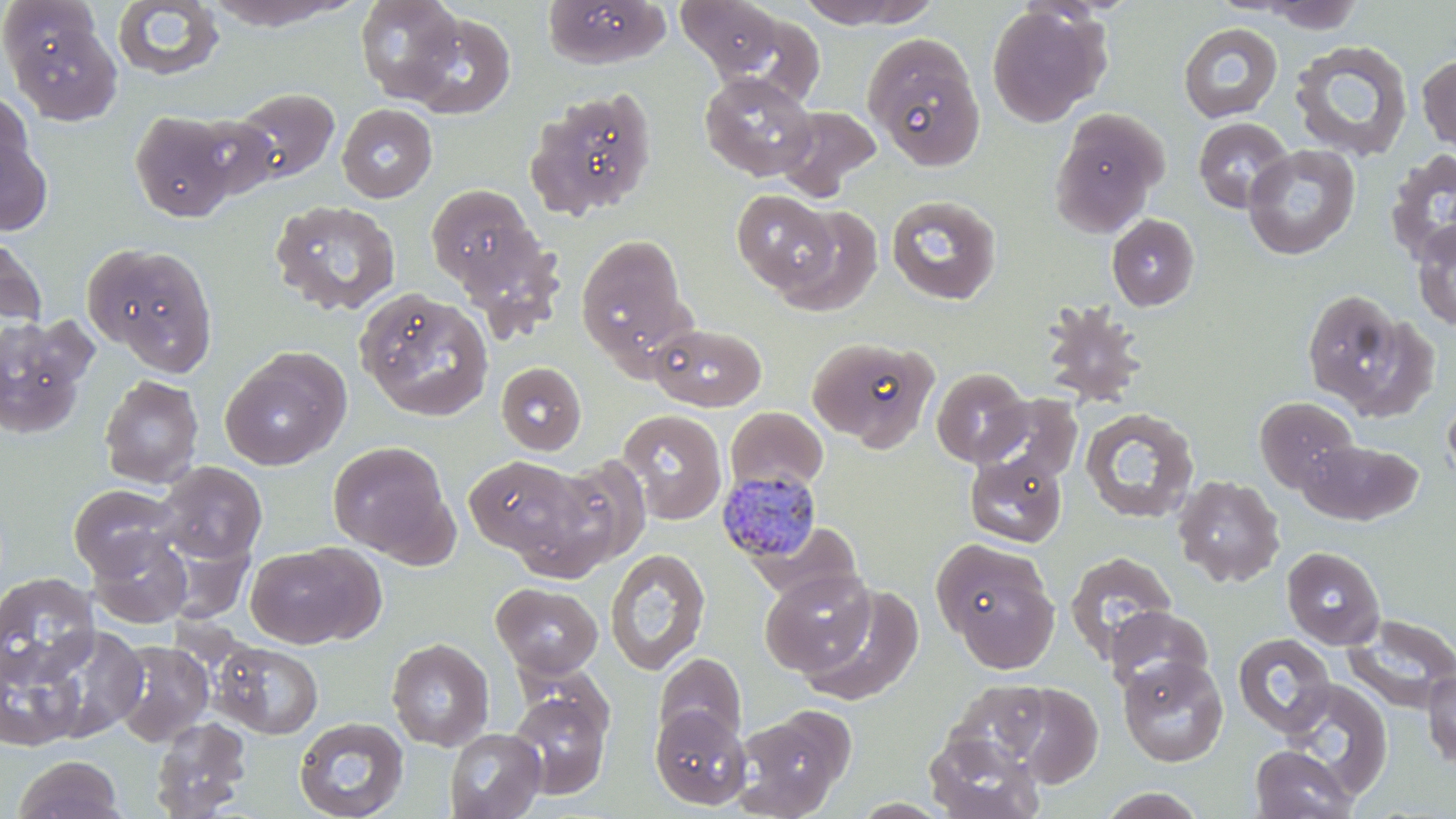

Approximate bounding boxes as named x1/y1/x2/y2 corners in pixels. Plasmodium malariae-infected red blood cell locations: (x1=717, y1=469, x2=825, y2=565). Uninfected red blood cell locations: (x1=355, y1=0, x2=464, y2=102), (x1=542, y1=0, x2=669, y2=68), (x1=676, y1=0, x2=788, y2=80), (x1=795, y1=0, x2=941, y2=29), (x1=0, y1=1, x2=103, y2=85), (x1=201, y1=1, x2=360, y2=30), (x1=1254, y1=1, x2=1366, y2=33), (x1=112, y1=2, x2=226, y2=82), (x1=986, y1=4, x2=1109, y2=127), (x1=405, y1=11, x2=516, y2=119), (x1=8, y1=16, x2=123, y2=126), (x1=1178, y1=23, x2=1283, y2=123), (x1=862, y1=33, x2=986, y2=170), (x1=1289, y1=40, x2=1414, y2=161), (x1=1417, y1=52, x2=1456, y2=153), (x1=699, y1=70, x2=817, y2=181), (x1=231, y1=87, x2=340, y2=185), (x1=526, y1=87, x2=658, y2=220), (x1=0, y1=90, x2=34, y2=190), (x1=337, y1=103, x2=437, y2=203), (x1=775, y1=105, x2=882, y2=200), (x1=1049, y1=108, x2=1168, y2=236), (x1=129, y1=111, x2=240, y2=222), (x1=182, y1=113, x2=280, y2=201), (x1=1193, y1=117, x2=1294, y2=213), (x1=0, y1=127, x2=52, y2=237), (x1=1242, y1=144, x2=1361, y2=261), (x1=1384, y1=149, x2=1456, y2=266), (x1=425, y1=183, x2=544, y2=296), (x1=731, y1=189, x2=838, y2=295), (x1=885, y1=195, x2=1002, y2=305), (x1=269, y1=199, x2=401, y2=316), (x1=771, y1=204, x2=884, y2=316), (x1=1106, y1=214, x2=1199, y2=311), (x1=1411, y1=219, x2=1456, y2=331), (x1=0, y1=230, x2=46, y2=330), (x1=576, y1=234, x2=689, y2=360), (x1=82, y1=241, x2=219, y2=374), (x1=1302, y1=288, x2=1428, y2=416), (x1=356, y1=289, x2=494, y2=422), (x1=1039, y1=300, x2=1147, y2=408), (x1=0, y1=315, x2=94, y2=440), (x1=649, y1=322, x2=766, y2=411), (x1=806, y1=336, x2=939, y2=450), (x1=220, y1=347, x2=351, y2=470), (x1=496, y1=361, x2=587, y2=455), (x1=931, y1=367, x2=1031, y2=467), (x1=98, y1=374, x2=203, y2=489), (x1=1442, y1=392, x2=1456, y2=491), (x1=975, y1=394, x2=1083, y2=486), (x1=1255, y1=396, x2=1359, y2=492), (x1=1079, y1=407, x2=1199, y2=524), (x1=726, y1=408, x2=829, y2=496), (x1=617, y1=409, x2=727, y2=524), (x1=1299, y1=439, x2=1423, y2=526), (x1=327, y1=441, x2=453, y2=560), (x1=964, y1=453, x2=1067, y2=548), (x1=463, y1=454, x2=587, y2=558), (x1=538, y1=456, x2=651, y2=573), (x1=156, y1=461, x2=267, y2=563), (x1=1173, y1=474, x2=1285, y2=587), (x1=68, y1=484, x2=182, y2=580), (x1=748, y1=521, x2=862, y2=606), (x1=88, y1=530, x2=193, y2=629), (x1=934, y1=540, x2=1059, y2=669), (x1=244, y1=543, x2=378, y2=648), (x1=1282, y1=546, x2=1385, y2=649), (x1=605, y1=548, x2=711, y2=675), (x1=1064, y1=551, x2=1178, y2=659), (x1=760, y1=568, x2=876, y2=676), (x1=0, y1=572, x2=100, y2=688), (x1=492, y1=582, x2=603, y2=677), (x1=798, y1=584, x2=924, y2=706), (x1=1105, y1=605, x2=1214, y2=695), (x1=1344, y1=614, x2=1456, y2=713), (x1=31, y1=624, x2=148, y2=742), (x1=1232, y1=632, x2=1336, y2=737), (x1=387, y1=638, x2=494, y2=751), (x1=0, y1=640, x2=88, y2=752), (x1=110, y1=640, x2=215, y2=746), (x1=213, y1=641, x2=323, y2=739), (x1=654, y1=653, x2=747, y2=747), (x1=1118, y1=656, x2=1229, y2=767), (x1=1422, y1=666, x2=1456, y2=771), (x1=946, y1=678, x2=1055, y2=769), (x1=1277, y1=679, x2=1393, y2=801), (x1=1003, y1=682, x2=1102, y2=786), (x1=507, y1=687, x2=611, y2=799), (x1=650, y1=705, x2=751, y2=810), (x1=734, y1=705, x2=854, y2=818), (x1=150, y1=716, x2=252, y2=819), (x1=294, y1=716, x2=409, y2=819), (x1=444, y1=728, x2=545, y2=819), (x1=924, y1=731, x2=1045, y2=819), (x1=1249, y1=745, x2=1358, y2=818), (x1=13, y1=754, x2=124, y2=819), (x1=1097, y1=787, x2=1209, y2=818). Slide-level diagnosis: Plasmodium malariae. Captured at 1000x magnification. Image is 1456×819 pixels. Thin blood film. Single field of view. Optical microscopy. May-Grünwald-Giemsa stain.